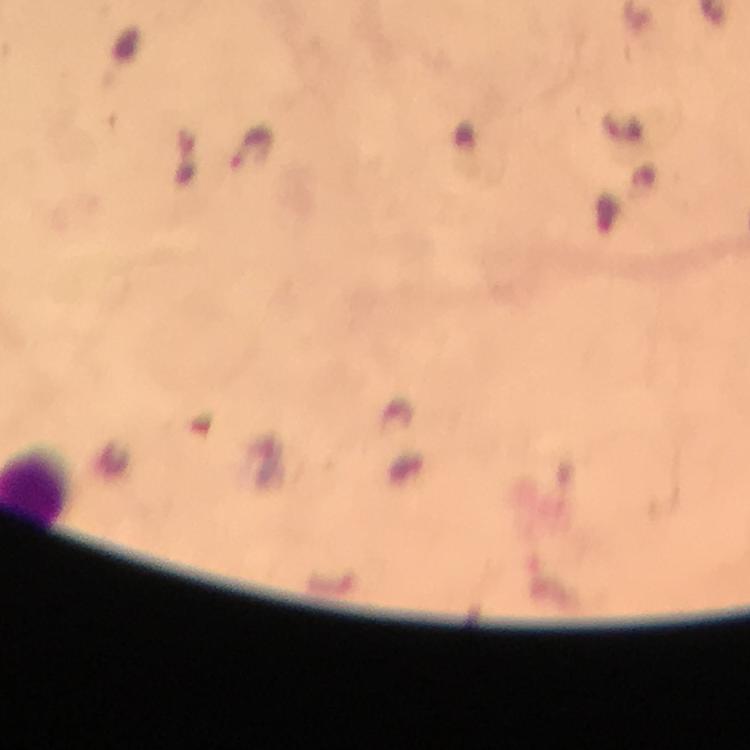
stain: Giemsa
magnification: 100x
capture: smartphone mounted on the microscope
immersion_oil: used
image_size: 750×750 pixels
cropped_from: a single field of view
context: from a diagnostic examination for malaria
plasmodium_parasite_locations: 'approximate centers as {x, y} in pixels: {250, 148}'
preparation: thick smear